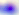
Toxoplasma gondii is seen. Captured at 400x magnification. Photomicrograph.